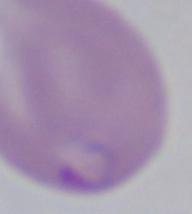
Summary:
  - Modality: photomicrograph
  - Identification: Babesia
  - Magnification: 1000x